Outline each blood parasite and name the species.
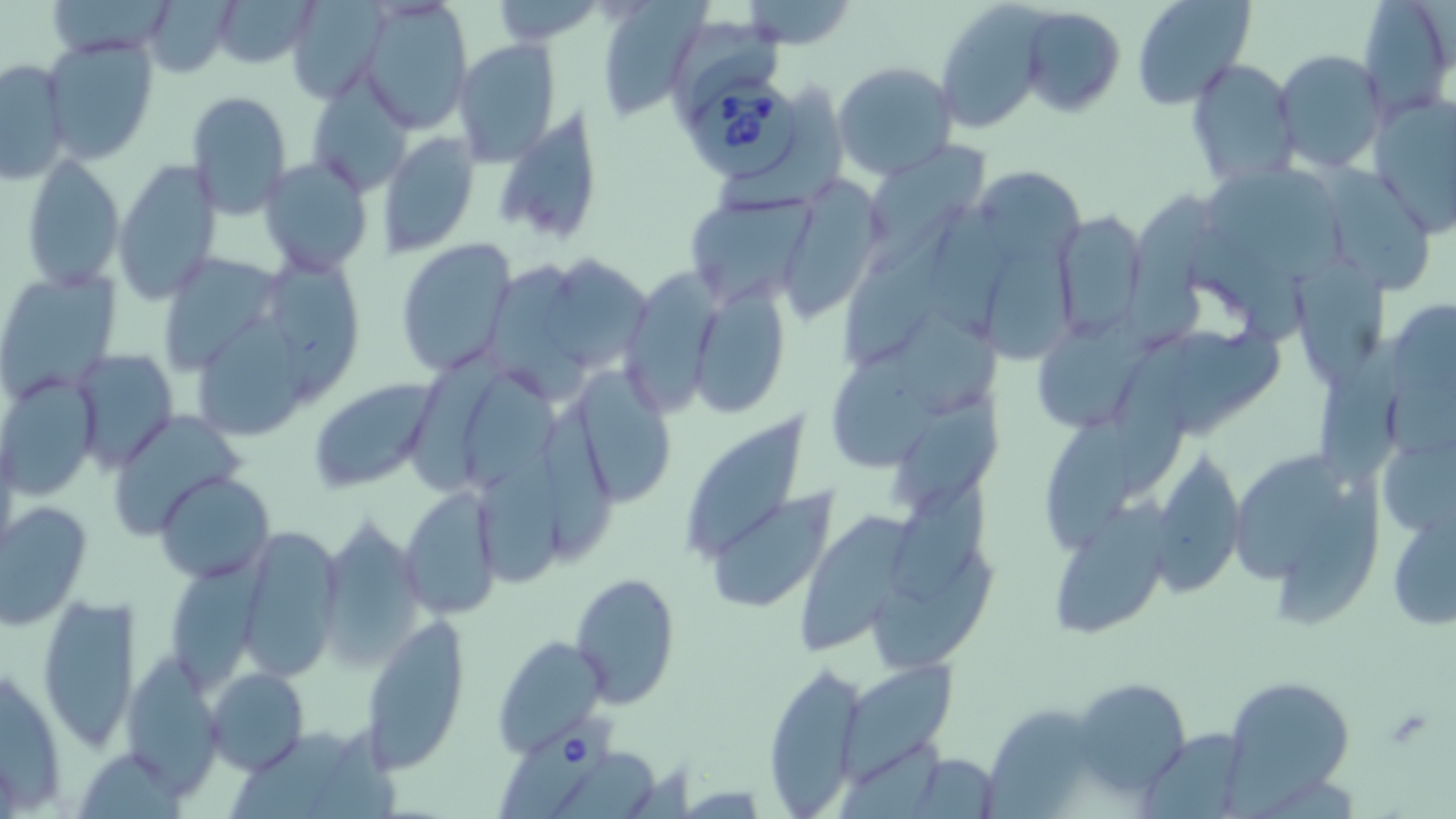
Approximate bounding boxes as named x1/y1/x2/y2 corners in pixels.
Babesia divergens-infected red blood cells: (x1=691, y1=81, x2=800, y2=181), (x1=497, y1=713, x2=614, y2=817).
No Plasmodium falciparum, Plasmodium ovale, Plasmodium malariae, Plasmodium vivax, or Trypanosoma brucei observed.

slide-level diagnosis = Babesia divergens
magnification = 1000x
image size = 1456×819 pixels
stain = May-Grünwald-Giemsa
modality = light microscopy
field of view = one of a larger specimen
uninfected red blood cell locations = approximate bounding boxes as named x1/y1/x2/y2 corners in pixels: (x1=210, y1=0, x2=322, y2=68), (x1=593, y1=0, x2=701, y2=121), (x1=1131, y1=0, x2=1256, y2=111), (x1=1357, y1=0, x2=1454, y2=118), (x1=144, y1=1, x2=235, y2=77), (x1=286, y1=1, x2=391, y2=103), (x1=491, y1=1, x2=601, y2=46), (x1=359, y1=2, x2=475, y2=129), (x1=741, y1=3, x2=857, y2=47), (x1=935, y1=3, x2=1049, y2=131), (x1=1017, y1=6, x2=1127, y2=117), (x1=674, y1=25, x2=787, y2=107), (x1=42, y1=35, x2=159, y2=164), (x1=451, y1=39, x2=562, y2=164), (x1=1274, y1=50, x2=1389, y2=174), (x1=0, y1=58, x2=71, y2=185), (x1=1186, y1=58, x2=1300, y2=188), (x1=832, y1=60, x2=958, y2=179), (x1=308, y1=73, x2=413, y2=198), (x1=186, y1=91, x2=292, y2=217), (x1=1367, y1=94, x2=1456, y2=236), (x1=492, y1=106, x2=606, y2=242), (x1=376, y1=133, x2=479, y2=258), (x1=863, y1=140, x2=987, y2=267), (x1=20, y1=153, x2=125, y2=291), (x1=259, y1=157, x2=373, y2=274), (x1=114, y1=160, x2=222, y2=306), (x1=1316, y1=163, x2=1437, y2=296), (x1=977, y1=167, x2=1085, y2=263), (x1=1217, y1=171, x2=1353, y2=286), (x1=776, y1=177, x2=882, y2=317), (x1=683, y1=191, x2=818, y2=306), (x1=1131, y1=193, x2=1217, y2=344), (x1=842, y1=205, x2=965, y2=378), (x1=1052, y1=212, x2=1147, y2=340), (x1=395, y1=237, x2=519, y2=378), (x1=988, y1=245, x2=1082, y2=361), (x1=161, y1=249, x2=285, y2=368), (x1=543, y1=254, x2=654, y2=373), (x1=269, y1=256, x2=359, y2=405), (x1=1286, y1=257, x2=1390, y2=385), (x1=493, y1=264, x2=586, y2=395), (x1=622, y1=266, x2=732, y2=420), (x1=1, y1=269, x2=120, y2=398), (x1=684, y1=282, x2=792, y2=419), (x1=892, y1=308, x2=1002, y2=419), (x1=193, y1=314, x2=312, y2=440), (x1=1039, y1=317, x2=1163, y2=422), (x1=1174, y1=324, x2=1290, y2=434), (x1=1117, y1=336, x2=1200, y2=489), (x1=1321, y1=339, x2=1416, y2=488), (x1=399, y1=343, x2=512, y2=492), (x1=828, y1=344, x2=943, y2=470), (x1=69, y1=347, x2=179, y2=469), (x1=569, y1=367, x2=679, y2=503), (x1=466, y1=369, x2=563, y2=485), (x1=0, y1=376, x2=98, y2=499), (x1=308, y1=377, x2=443, y2=492), (x1=896, y1=397, x2=1011, y2=508), (x1=684, y1=403, x2=806, y2=562), (x1=113, y1=409, x2=244, y2=542), (x1=547, y1=414, x2=619, y2=555), (x1=1045, y1=414, x2=1138, y2=551), (x1=480, y1=441, x2=574, y2=580), (x1=1152, y1=446, x2=1249, y2=598), (x1=1229, y1=452, x2=1353, y2=579), (x1=154, y1=471, x2=274, y2=585), (x1=896, y1=471, x2=1004, y2=610), (x1=399, y1=485, x2=505, y2=614), (x1=1279, y1=487, x2=1392, y2=631), (x1=705, y1=490, x2=837, y2=614), (x1=1056, y1=496, x2=1169, y2=636), (x1=1, y1=499, x2=91, y2=629), (x1=800, y1=499, x2=920, y2=651), (x1=1388, y1=509, x2=1455, y2=635), (x1=317, y1=515, x2=425, y2=664), (x1=243, y1=534, x2=342, y2=681), (x1=876, y1=543, x2=996, y2=671), (x1=170, y1=554, x2=286, y2=682), (x1=570, y1=572, x2=679, y2=707), (x1=37, y1=595, x2=140, y2=752), (x1=361, y1=620, x2=470, y2=771), (x1=490, y1=634, x2=608, y2=756), (x1=123, y1=652, x2=229, y2=792), (x1=1, y1=659, x2=70, y2=809), (x1=765, y1=659, x2=866, y2=815), (x1=842, y1=666, x2=957, y2=780), (x1=204, y1=668, x2=309, y2=774), (x1=1221, y1=675, x2=1358, y2=803), (x1=1072, y1=677, x2=1192, y2=798), (x1=978, y1=703, x2=1111, y2=816), (x1=1140, y1=728, x2=1250, y2=819), (x1=906, y1=757, x2=1002, y2=815)
preparation = thin blood smear